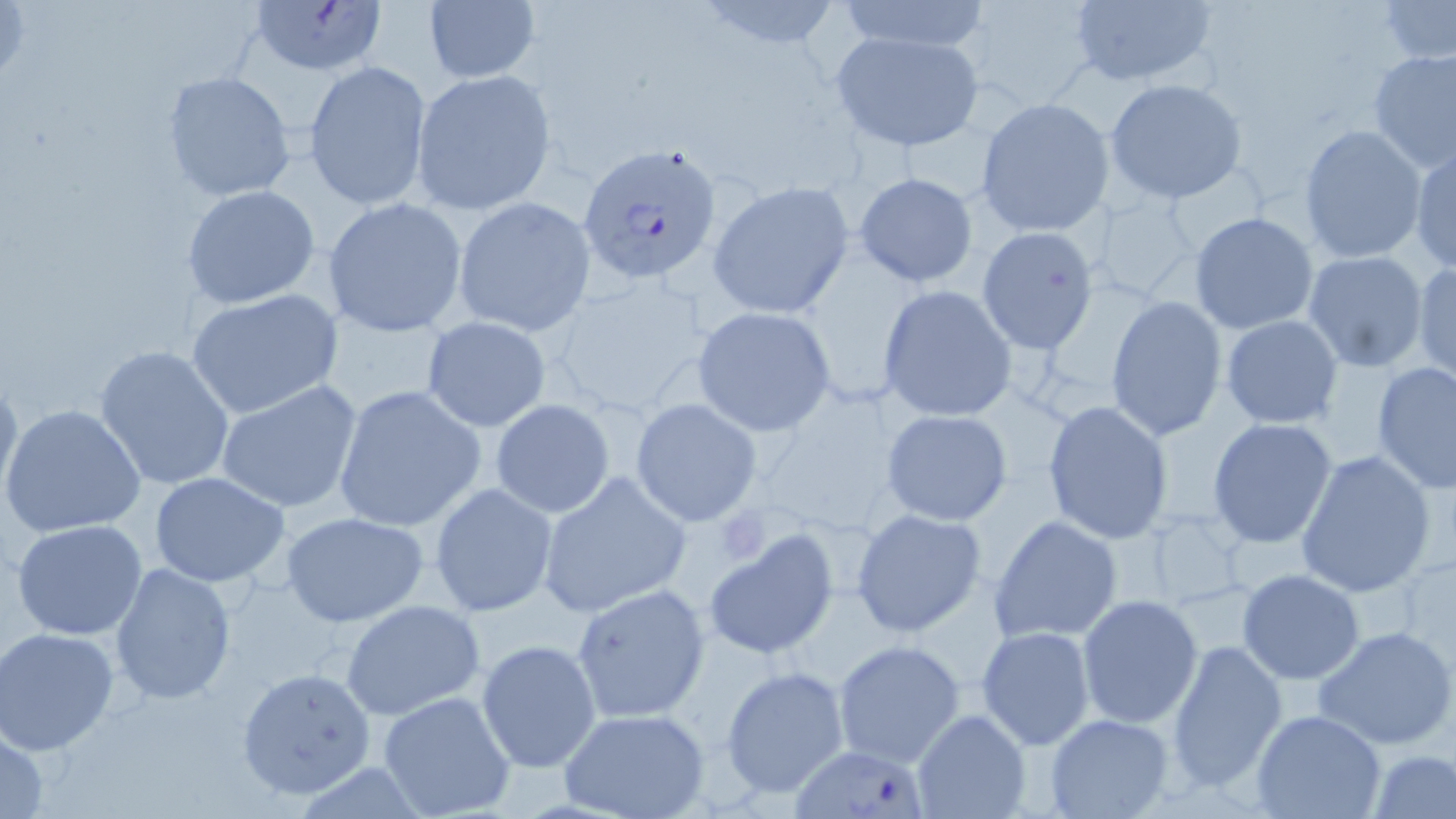
{
  "slide_level_diagnosis": "Plasmodium falciparum",
  "stain": "May-Grünwald-Giemsa",
  "field_of_view": "one of a larger specimen",
  "uninfected_red_blood_cell_locations": "approximate bounding boxes as [x1, y1, x2, y2] in pixels: [693, 0, 847, 55], [836, 0, 993, 55], [1065, 1, 1220, 88], [1377, 1, 1455, 66], [422, 2, 541, 84], [828, 28, 986, 153], [1367, 47, 1456, 172], [304, 59, 433, 211], [412, 69, 556, 212], [162, 71, 295, 201], [1104, 78, 1249, 204], [975, 98, 1114, 237], [1300, 124, 1426, 263], [1410, 143, 1455, 274], [854, 172, 980, 287], [708, 182, 854, 319], [180, 184, 321, 310], [453, 196, 596, 337], [322, 197, 468, 337], [1190, 212, 1319, 335], [976, 227, 1099, 355], [1302, 251, 1429, 373], [1363, 254, 1456, 383], [1412, 259, 1456, 386], [877, 285, 1018, 423], [187, 290, 343, 418], [1106, 294, 1227, 441], [691, 305, 839, 436], [1220, 315, 1345, 429], [421, 316, 550, 431], [94, 344, 235, 490], [1371, 360, 1456, 494], [0, 368, 22, 510], [214, 380, 363, 512], [333, 385, 485, 532], [489, 399, 616, 519], [631, 399, 762, 527], [1043, 399, 1174, 545], [2, 404, 146, 537], [881, 409, 1013, 526], [1207, 417, 1339, 549], [1295, 449, 1437, 599], [150, 472, 294, 589], [537, 473, 691, 618], [430, 482, 560, 617], [851, 508, 987, 638], [280, 511, 428, 627], [990, 515, 1124, 645], [11, 519, 148, 641], [702, 529, 841, 660], [109, 562, 236, 706], [1237, 568, 1365, 683], [571, 583, 711, 723], [1076, 594, 1203, 729], [340, 599, 486, 721], [1312, 625, 1456, 752], [976, 626, 1098, 750], [0, 628, 121, 756], [476, 639, 603, 773], [832, 639, 966, 767], [1166, 639, 1287, 792], [721, 665, 851, 800], [236, 667, 377, 799], [376, 689, 517, 818], [913, 709, 1031, 818], [560, 710, 710, 819], [1251, 710, 1386, 818], [1046, 713, 1174, 819], [1, 723, 50, 818], [1367, 748, 1455, 819]",
  "modality": "light microscopy",
  "image_size": "1456×819 pixels",
  "plasmodium_falciparum_infected_red_blood_cell_locations": "approximate bounding boxes as [x1, y1, x2, y2] in pixels: [246, 0, 387, 77], [577, 140, 724, 289], [790, 744, 944, 819]",
  "magnification": "1000x",
  "preparation": "thin blood film",
  "platelet_locations": "approximate bounding boxes as [x1, y1, x2, y2] in pixels: [716, 510, 774, 564]"
}